Assess the morphology of the erythrocytes.
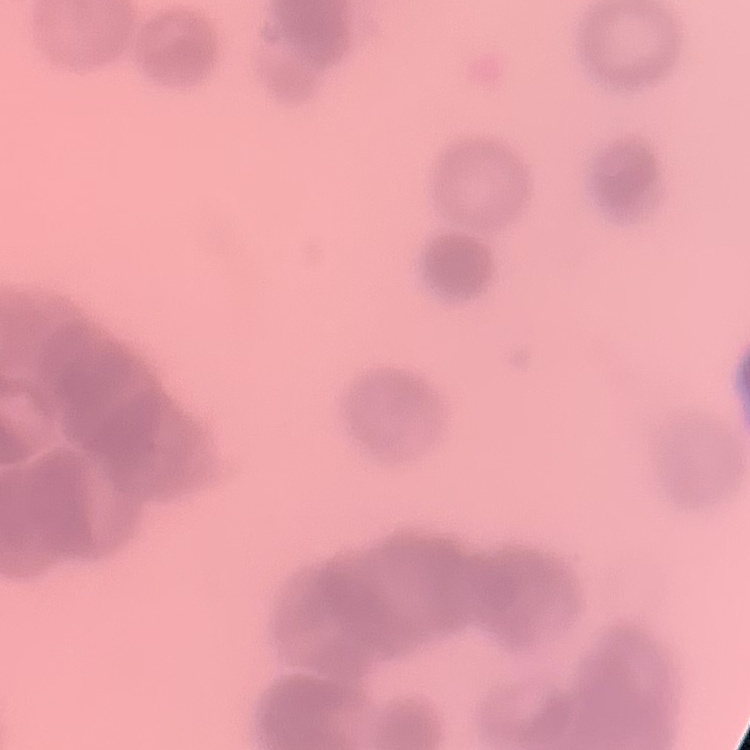
Rouleaux formation.

{
  "preparation": "thin blood film",
  "stain": "Field's or Giemsa",
  "image_type": "square crop of a larger photomicrograph"
}